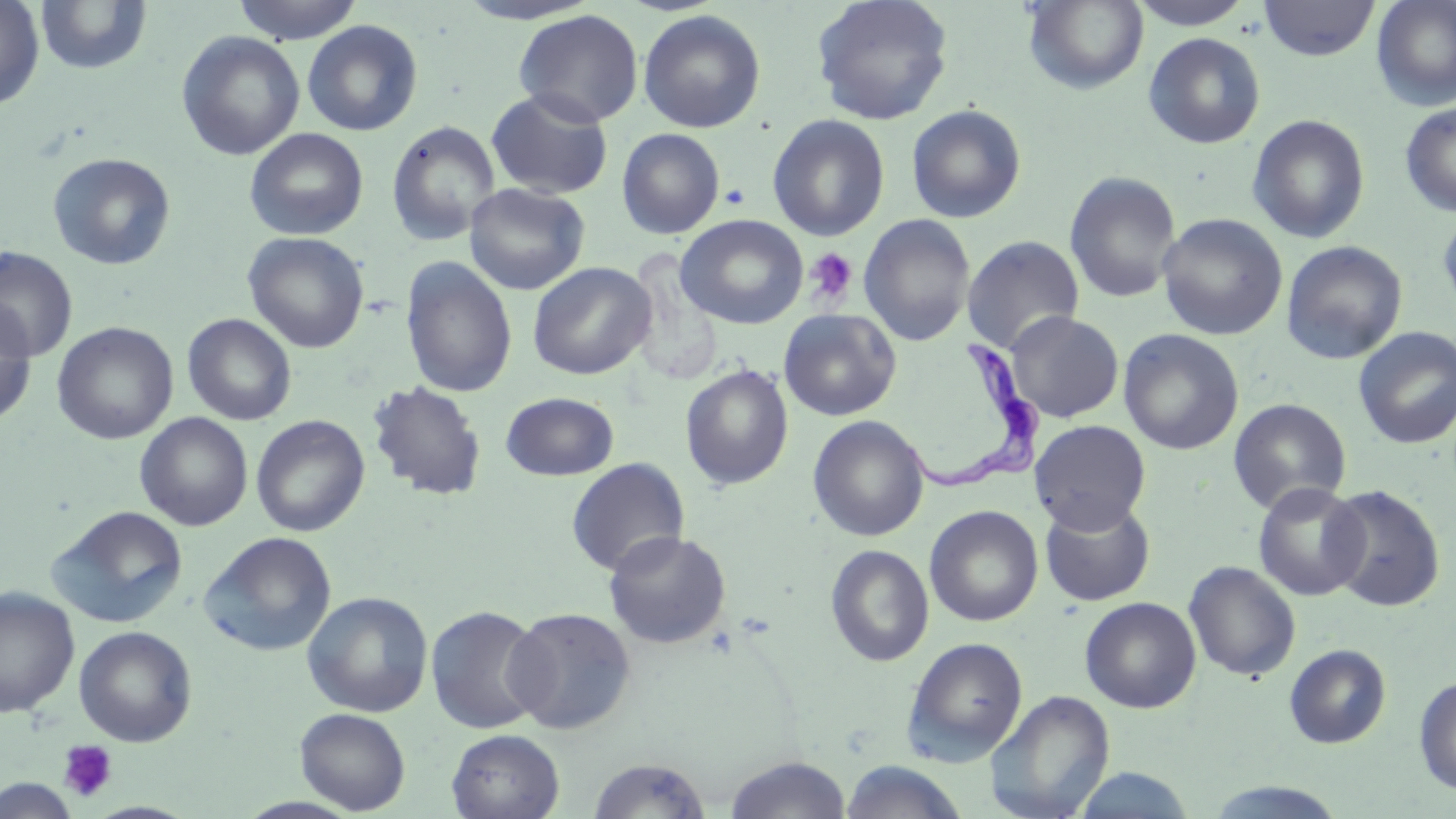
slide-level diagnosis = Trypanosoma brucei
modality = optical microscopy
Trypanosoma brucei locations = approximate bounding boxes as named x1/y1/x2/y2 corners in pixels: (x1=903, y1=336, x2=1048, y2=496)
stain = May-Grünwald-Giemsa
magnification = 1000x
uninfected red blood cell locations = approximate bounding boxes as named x1/y1/x2/y2 corners in pixels: (x1=0, y1=0, x2=44, y2=110), (x1=232, y1=0, x2=364, y2=43), (x1=452, y1=0, x2=604, y2=25), (x1=810, y1=0, x2=954, y2=126), (x1=1022, y1=0, x2=1149, y2=95), (x1=1130, y1=0, x2=1254, y2=30), (x1=1259, y1=0, x2=1380, y2=61), (x1=1372, y1=0, x2=1456, y2=111), (x1=35, y1=1, x2=153, y2=77), (x1=513, y1=9, x2=644, y2=128), (x1=638, y1=10, x2=766, y2=133), (x1=302, y1=20, x2=423, y2=136), (x1=176, y1=30, x2=305, y2=161), (x1=1143, y1=32, x2=1266, y2=149), (x1=485, y1=88, x2=614, y2=200), (x1=1399, y1=101, x2=1456, y2=216), (x1=906, y1=104, x2=1027, y2=224), (x1=768, y1=114, x2=890, y2=241), (x1=1247, y1=114, x2=1370, y2=243), (x1=386, y1=120, x2=501, y2=245), (x1=244, y1=128, x2=368, y2=241), (x1=617, y1=128, x2=725, y2=239), (x1=47, y1=152, x2=176, y2=270), (x1=1064, y1=171, x2=1182, y2=304), (x1=464, y1=183, x2=590, y2=296), (x1=1437, y1=205, x2=1456, y2=318), (x1=859, y1=213, x2=976, y2=347), (x1=1156, y1=213, x2=1288, y2=340), (x1=676, y1=215, x2=809, y2=329), (x1=243, y1=231, x2=370, y2=353), (x1=962, y1=235, x2=1085, y2=355), (x1=1281, y1=241, x2=1408, y2=365), (x1=0, y1=247, x2=78, y2=363), (x1=400, y1=256, x2=518, y2=399), (x1=528, y1=261, x2=656, y2=379), (x1=0, y1=298, x2=36, y2=427), (x1=778, y1=308, x2=902, y2=421), (x1=1006, y1=310, x2=1124, y2=423), (x1=182, y1=313, x2=297, y2=426), (x1=52, y1=322, x2=178, y2=445), (x1=1353, y1=326, x2=1456, y2=450), (x1=1118, y1=328, x2=1244, y2=455), (x1=680, y1=364, x2=794, y2=489), (x1=367, y1=380, x2=487, y2=501), (x1=501, y1=392, x2=619, y2=481), (x1=1228, y1=398, x2=1351, y2=516), (x1=135, y1=413, x2=253, y2=530), (x1=251, y1=415, x2=370, y2=536), (x1=808, y1=415, x2=930, y2=542), (x1=1030, y1=419, x2=1151, y2=534), (x1=566, y1=457, x2=689, y2=577), (x1=1252, y1=481, x2=1370, y2=601), (x1=1323, y1=484, x2=1446, y2=611), (x1=1039, y1=498, x2=1156, y2=606), (x1=48, y1=505, x2=188, y2=628), (x1=924, y1=505, x2=1044, y2=627), (x1=603, y1=530, x2=731, y2=649), (x1=199, y1=531, x2=337, y2=657), (x1=825, y1=544, x2=934, y2=667), (x1=1183, y1=560, x2=1301, y2=682), (x1=0, y1=586, x2=80, y2=717), (x1=302, y1=591, x2=434, y2=717), (x1=1079, y1=597, x2=1201, y2=713), (x1=425, y1=604, x2=548, y2=735), (x1=503, y1=606, x2=636, y2=734), (x1=74, y1=626, x2=198, y2=747), (x1=902, y1=636, x2=1029, y2=764), (x1=1284, y1=644, x2=1391, y2=749), (x1=1413, y1=676, x2=1456, y2=796), (x1=985, y1=689, x2=1115, y2=819), (x1=295, y1=708, x2=410, y2=814), (x1=446, y1=729, x2=564, y2=819), (x1=723, y1=756, x2=853, y2=818), (x1=587, y1=757, x2=711, y2=818), (x1=839, y1=760, x2=969, y2=819), (x1=1069, y1=767, x2=1200, y2=818), (x1=1, y1=774, x2=79, y2=818), (x1=1200, y1=780, x2=1351, y2=818)
image size = 1456×819 pixels
field of view = one of a larger specimen
preparation = thin blood smear
platelet locations = approximate bounding boxes as named x1/y1/x2/y2 corners in pixels: (x1=804, y1=247, x2=858, y2=307), (x1=58, y1=739, x2=118, y2=802)